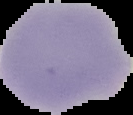

Image is 133×115 pixels. Malaria status: uninfected. Cell region segmented out of the field of view; the surrounding area is masked to black. From a thin blood smear.